Classify this cell by malaria status.
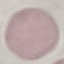

It is uninfected.

Summary:
  - Stain: Giemsa
  - Image type: automatically extracted cell patch, resized to 64 × 64 pixels
  - Preparation: thin blood smear
  - Capture: smartphone through the microscope eyepiece